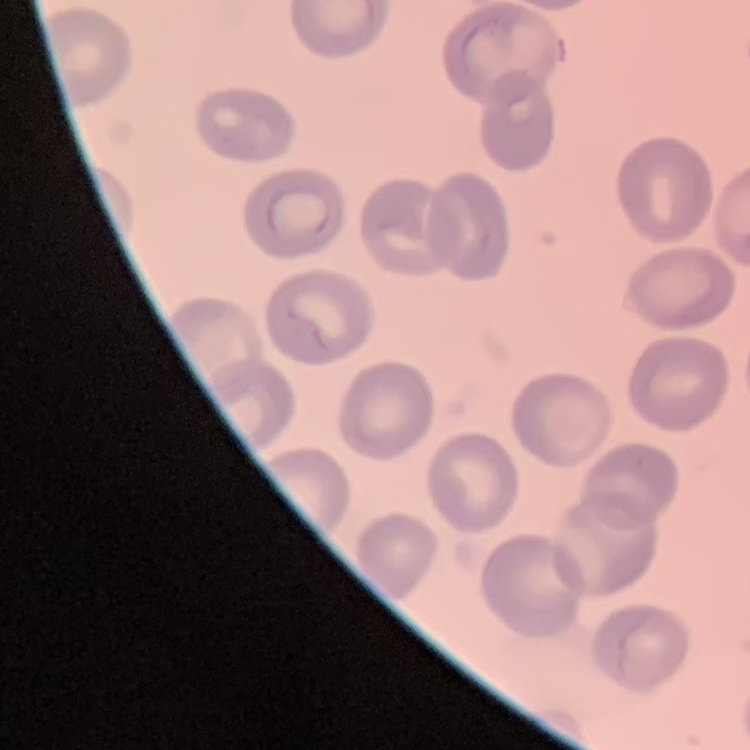

Summary:
  - Erythrocyte morphology: no rouleaux formation
  - Image type: one tile cut from a larger photomicrograph
  - Stain: Field's or Giemsa
  - Preparation: thin blood film